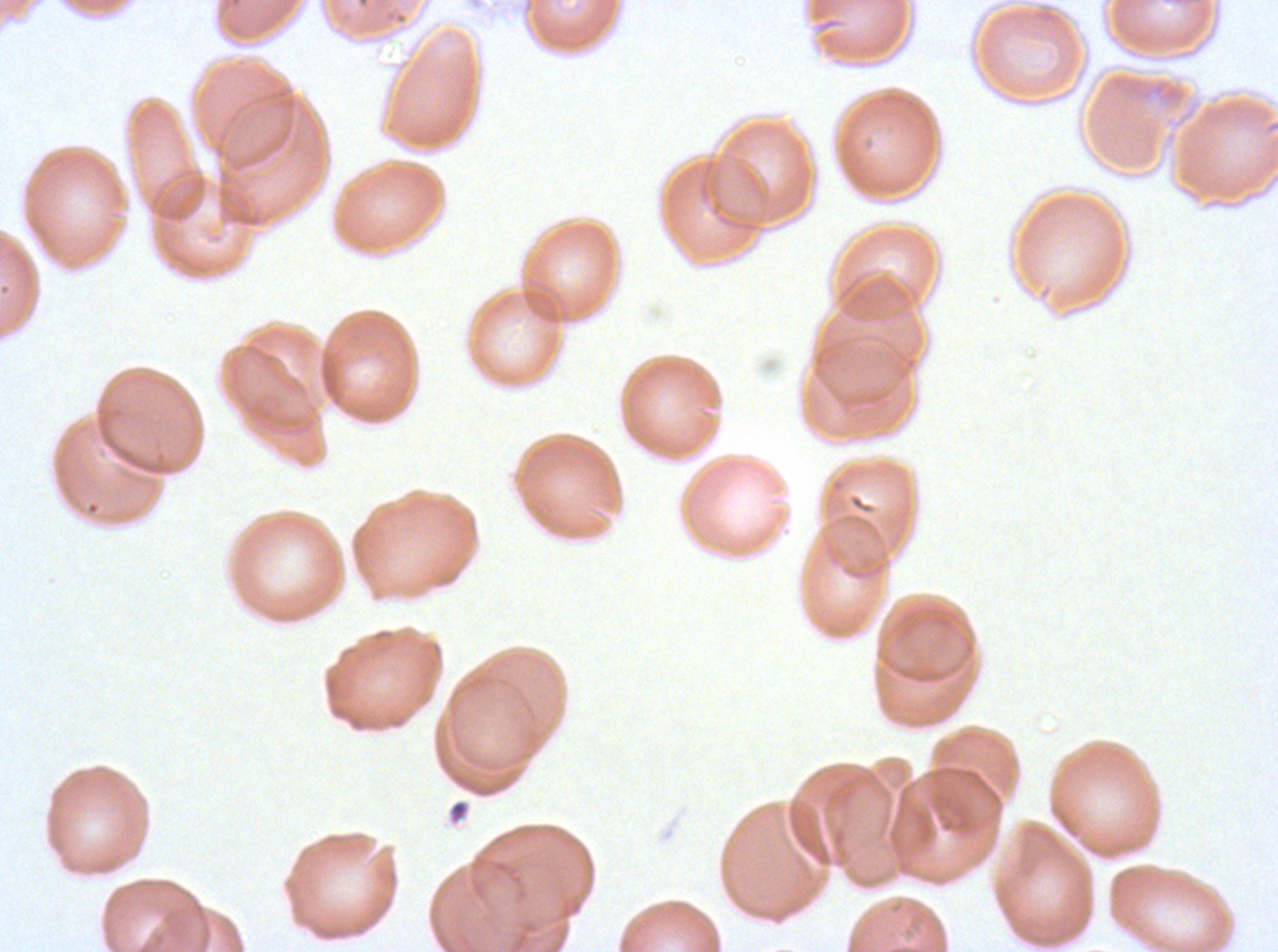

Approximate bounding boxes as (x1, y1, x2, y2) in pixels. Debris locations: (447, 799, 470, 825). Image is 1278×952 pixels. Thin blood film. Plasmodium falciparum cultured ex vivo for 24 to 48 hours, from a patient in The Gambia. Giemsa-stained preparation. A sub-image separated from a larger composite.